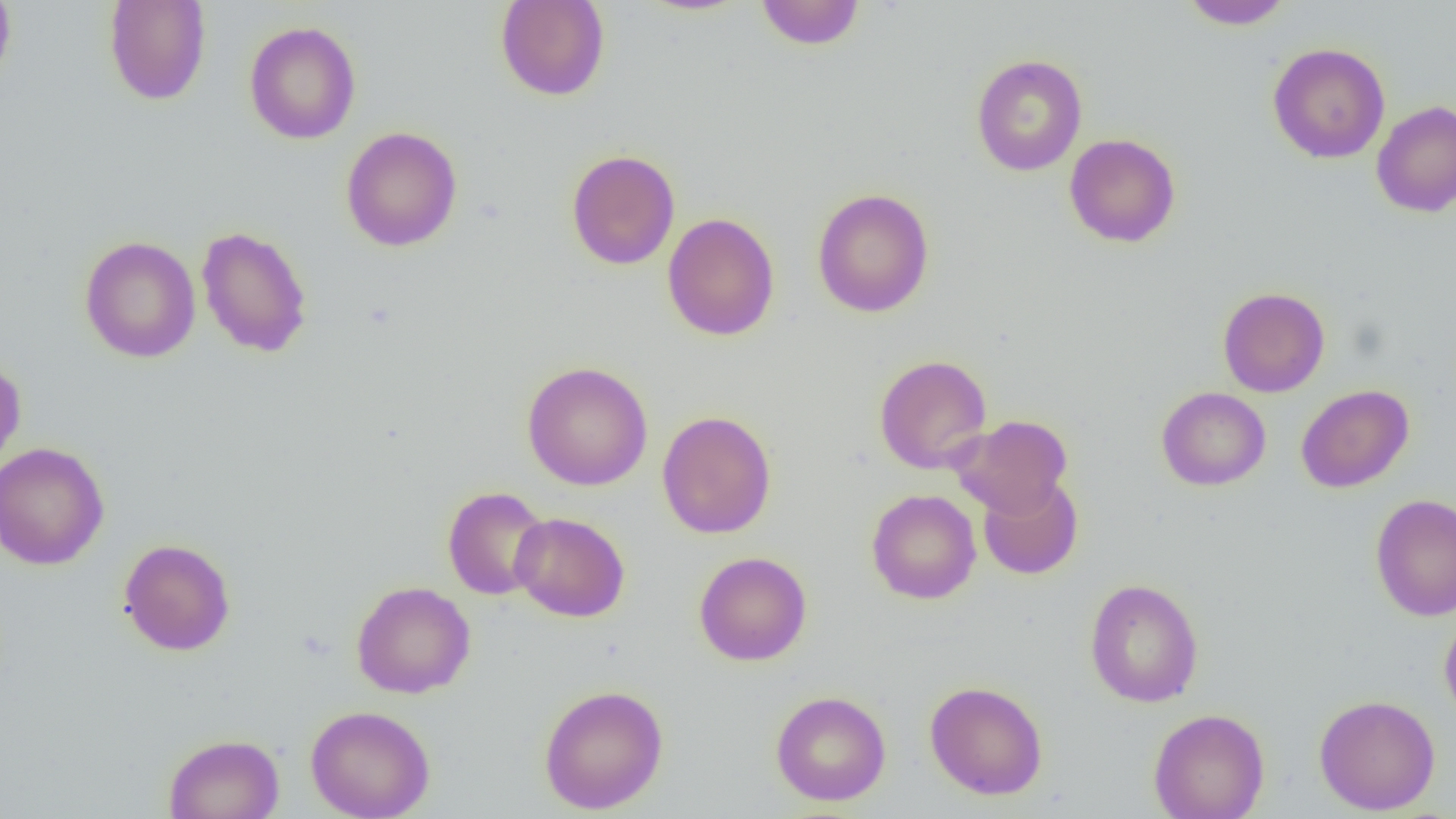
Summary:
  - Coordinate format: approximate bounding boxes as (x1, y1, x2, y2) in pixels
  - Uninfected red blood cell locations: (0, 0, 17, 89), (103, 0, 212, 106), (495, 0, 611, 101), (755, 0, 866, 50), (1180, 0, 1294, 30), (243, 20, 361, 145), (1267, 42, 1390, 163), (971, 53, 1087, 176), (1371, 100, 1456, 218), (341, 126, 463, 252), (1064, 133, 1181, 247), (566, 149, 680, 270), (812, 188, 935, 318), (663, 212, 780, 341), (196, 225, 313, 358), (79, 235, 201, 363), (1217, 286, 1330, 397), (874, 354, 992, 474), (0, 356, 27, 477), (522, 361, 653, 491), (1296, 384, 1414, 492), (1156, 386, 1271, 491), (657, 410, 777, 539), (951, 414, 1073, 518), (0, 442, 110, 570), (976, 474, 1083, 580), (442, 486, 551, 600), (866, 488, 981, 604), (1370, 492, 1456, 621), (510, 512, 630, 622), (118, 538, 236, 656), (694, 552, 812, 666), (1084, 578, 1204, 708), (350, 581, 476, 698), (1439, 612, 1456, 726), (924, 680, 1048, 800), (539, 684, 669, 814), (770, 690, 891, 806), (1314, 694, 1441, 815), (305, 704, 435, 819), (1148, 708, 1270, 819), (163, 733, 284, 819)
  - Slide-level diagnosis: no evidence of blood parasites
  - Field of view: one of a larger specimen
  - Magnification: 1000x
  - Image size: 1456×819 pixels
  - Preparation: thin blood film
  - Modality: light microscopy